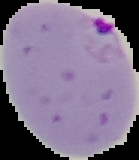

From a thin blood film. Image is 139×160 pixels. Cell region segmented out of the field of view; the surrounding area is masked to black. Result: Plasmodium parasites detected.